Locate every malaria parasite.
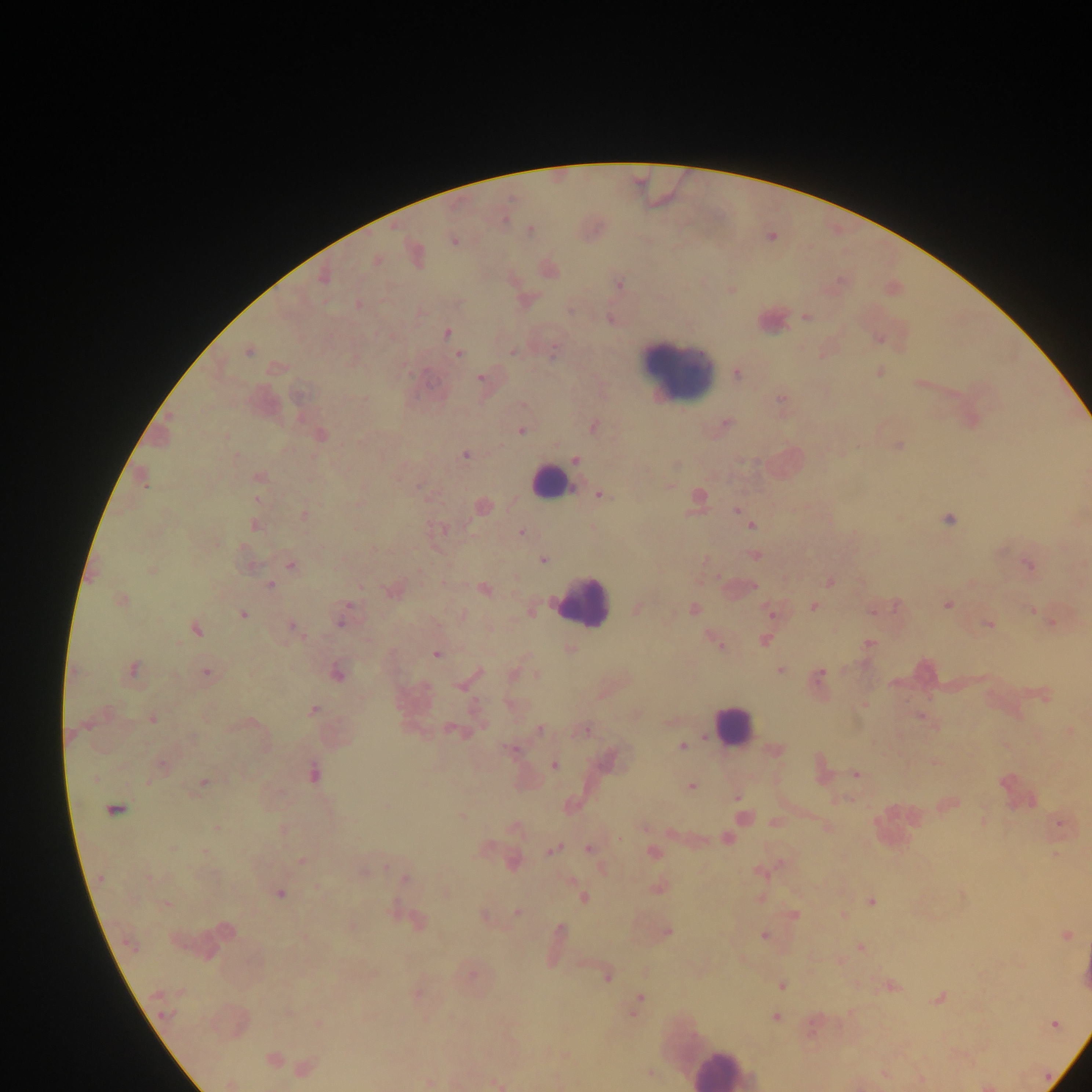

Approximate centers as [x, y] in pixels.
Malaria parasites: [529, 230], [453, 240], [415, 254], [375, 260], [548, 269], [324, 276], [618, 283], [731, 289], [357, 304], [805, 317], [610, 319], [446, 332], [878, 338], [248, 350], [553, 350], [459, 354], [878, 372], [737, 373], [480, 377], [920, 383], [781, 402], [971, 420], [725, 424], [593, 426], [521, 431], [320, 435], [897, 445], [465, 454], [575, 460], [258, 477], [141, 478], [668, 485], [599, 494], [696, 498], [482, 506], [736, 510], [304, 515], [949, 518], [253, 524], [751, 524], [521, 533], [754, 555], [542, 559], [290, 564], [248, 565], [1029, 565], [151, 569], [829, 581], [269, 585], [483, 588], [393, 589], [120, 600], [947, 603], [814, 606], [636, 608], [693, 609], [873, 609], [530, 610], [1032, 610], [770, 613], [242, 614], [343, 614], [462, 614], [1052, 622], [988, 624], [292, 626], [195, 628], [763, 639], [717, 642], [869, 643], [570, 650], [436, 653], [131, 670], [780, 671], [336, 672], [206, 673], [513, 673], [537, 675], [818, 675], [466, 682], [1042, 693], [863, 704], [313, 710], [920, 716], [152, 718], [671, 721], [454, 730], [540, 730], [583, 730], [1069, 731], [682, 746], [512, 749], [774, 751], [610, 758], [935, 762], [161, 765], [553, 765], [819, 769], [312, 773], [856, 774], [203, 782], [691, 785], [736, 797], [947, 804], [114, 808], [461, 816], [742, 818], [774, 822], [983, 822], [1058, 823], [643, 826], [515, 827], [827, 827], [217, 828], [283, 829], [726, 838], [485, 848], [553, 848], [589, 849], [653, 852], [1055, 854], [302, 861], [512, 861], [363, 870], [759, 870], [405, 878], [318, 887], [657, 887], [445, 892], [279, 893], [583, 897], [760, 897], [870, 902], [516, 911], [793, 914], [843, 915], [484, 916], [416, 921], [350, 926], [222, 930], [666, 931], [1064, 935], [763, 936], [556, 938], [860, 948], [471, 974], [607, 975], [781, 985], [890, 985], [416, 992], [939, 997], [636, 1002], [774, 1016], [318, 1023], [1054, 1024], [272, 1060], [303, 1068], [650, 1073], [884, 1073], [920, 1080], [428, 1082], [496, 1083], [230, 1084], [986, 1085].

Leukocyte locations: [771, 318], [677, 373], [551, 482], [582, 601], [731, 726], [721, 1067]. Single field of view. Image is 1092×1092 pixels. Sample from Ghana. Mobile-phone photograph taken through the microscope. Thick blood smear.